Identify the parasite.
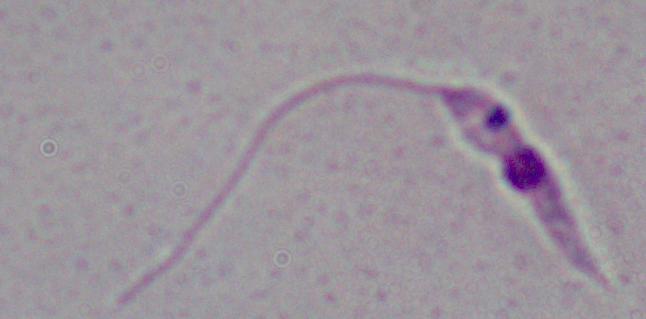
Leishmania.

Captured at 1000x magnification. Photomicrograph.